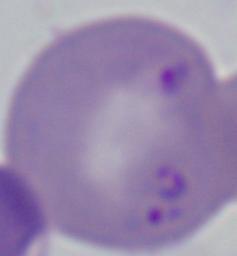

Summary:
  - Identification: Babesia
  - Magnification: 1000x
  - Modality: photomicrograph